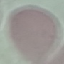 Result: no malaria parasites detected. Cell patch, automatically extracted from a larger field of view and resized to 64 × 64 pixels. Thin smear of blood. Giemsa stain. Photographed with a smartphone camera at the microscope eyepiece.